Assess this cell for malaria.
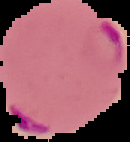
It is parasitized.

Summary:
  - Preparation: thin blood smear
  - Image type: segmented cell region on a black background
  - Image size: 130×142 pixels